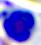

identification = leukocyte
magnification = 400x
modality = micrograph